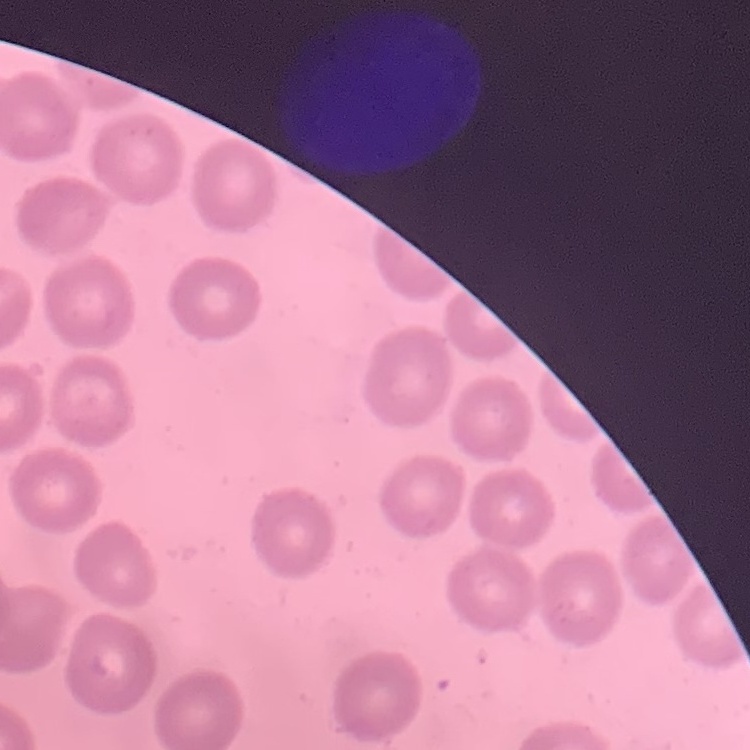

Summary:
  - Erythrocyte morphology: no rouleaux formation
  - Image type: square crop of a larger photomicrograph
  - Stain: Field's or Giemsa
  - Preparation: thin peripheral smear